Give the position of every malaria parasite and every leukocyte.
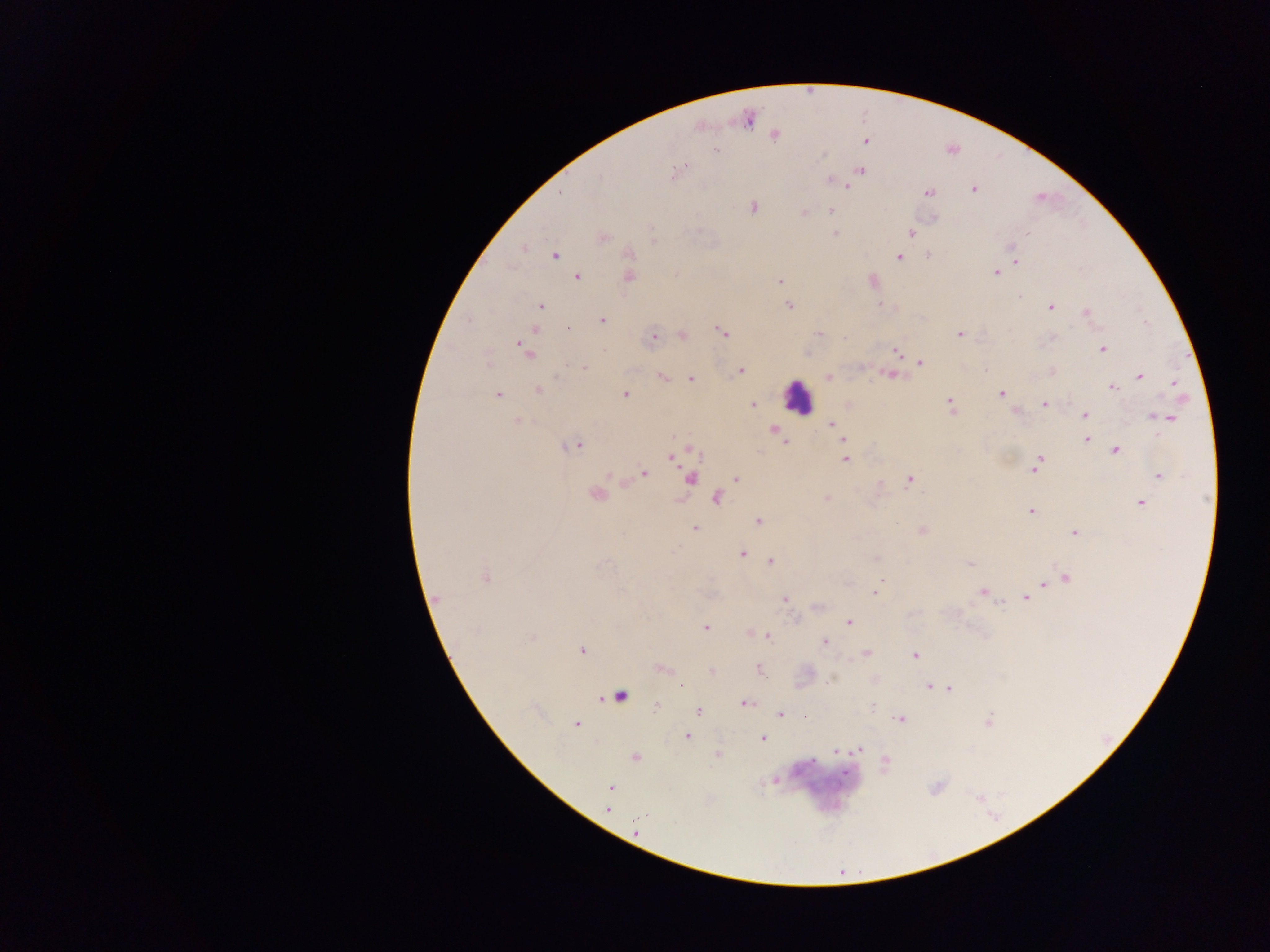
Approximate centers as {x, y} in pixels.
Malaria parasites: {749, 119}, {775, 136}, {866, 142}, {716, 151}, {681, 168}, {861, 170}, {676, 172}, {830, 181}, {842, 184}, {848, 186}, {973, 189}, {561, 192}, {928, 192}, {753, 207}, {831, 210}, {803, 213}, {934, 218}, {911, 233}, {835, 234}, {603, 238}, {652, 241}, {524, 247}, {1013, 248}, {630, 254}, {555, 256}, {929, 256}, {898, 258}, {1015, 261}, {995, 272}, {577, 277}, {628, 277}, {779, 281}, {879, 304}, {788, 305}, {540, 306}, {1050, 306}, {1087, 312}, {602, 320}, {567, 329}, {535, 330}, {723, 331}, {819, 333}, {959, 334}, {683, 336}, {653, 337}, {522, 345}, {1102, 349}, {896, 351}, {527, 352}, {920, 362}, {489, 363}, {584, 367}, {741, 371}, {1052, 371}, {890, 375}, {1140, 376}, {662, 377}, {828, 377}, {690, 379}, {1175, 383}, {1112, 387}, {537, 390}, {625, 394}, {1002, 394}, {498, 395}, {950, 401}, {1044, 404}, {752, 405}, {1085, 414}, {1153, 416}, {1168, 418}, {517, 420}, {832, 424}, {774, 428}, {837, 432}, {844, 440}, {1086, 440}, {786, 441}, {574, 446}, {1116, 449}, {694, 452}, {672, 456}, {845, 459}, {1039, 461}, {643, 473}, {609, 476}, {1159, 477}, {736, 478}, {690, 479}, {910, 480}, {594, 496}, {717, 499}, {826, 499}, {1140, 503}, {1031, 511}, {758, 521}, {695, 528}, {922, 531}, {1075, 532}, {742, 553}, {771, 561}, {969, 563}, {485, 577}, {1066, 578}, {1043, 584}, {983, 591}, {875, 593}, {1026, 597}, {439, 598}, {785, 599}, {1001, 604}, {848, 622}, {705, 627}, {767, 636}, {532, 639}, {824, 642}, {582, 650}, {866, 653}, {916, 655}, {661, 668}, {759, 669}, {712, 671}, {829, 681}, {681, 685}, {929, 687}, {949, 689}, {620, 696}, {744, 703}, {656, 706}, {872, 707}, {699, 712}, {780, 714}, {806, 717}, {901, 719}, {987, 720}, {576, 724}, {687, 736}, {763, 738}, {858, 750}, {836, 752}, {717, 754}, {635, 757}, {886, 761}, {775, 780}, {610, 787}, {607, 809}.
Leukocytes: {797, 396}.

preparation = thick blood smear
capture = mobile-phone photograph through a microscope
image size = 1270×952 pixels
country = Ghana
field of view = single